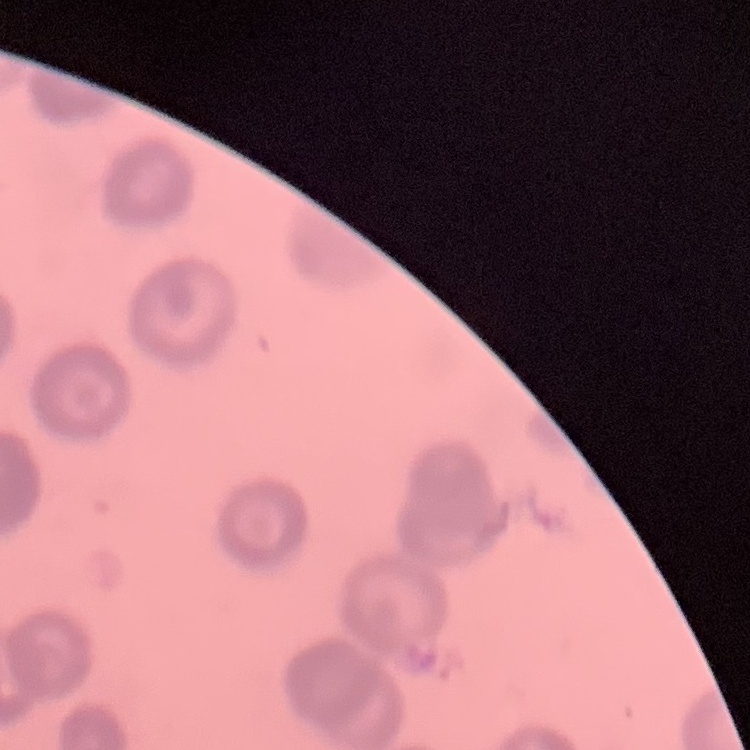
Summary:
  - Red blood cell morphology: rouleaux formation
  - Stain: Field's or Giemsa
  - Preparation: thin blood smear
  - Image type: one tile cut from a larger photomicrograph